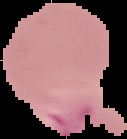
Malaria status: parasitized. From a thin blood film. Image is 127×139 pixels. Segmented cell region on a black background.